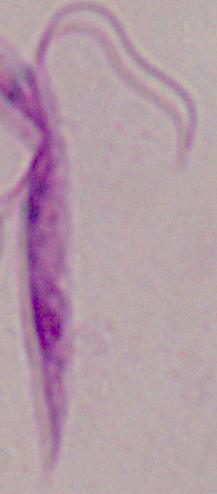
Summary:
  - Modality: photomicrograph
  - Identification: Leishmania
  - Magnification: 1000x